State which parasite is depicted.
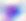
Toxoplasma gondii.

Photomicrograph. 400x magnification.